Name the blood parasite species.
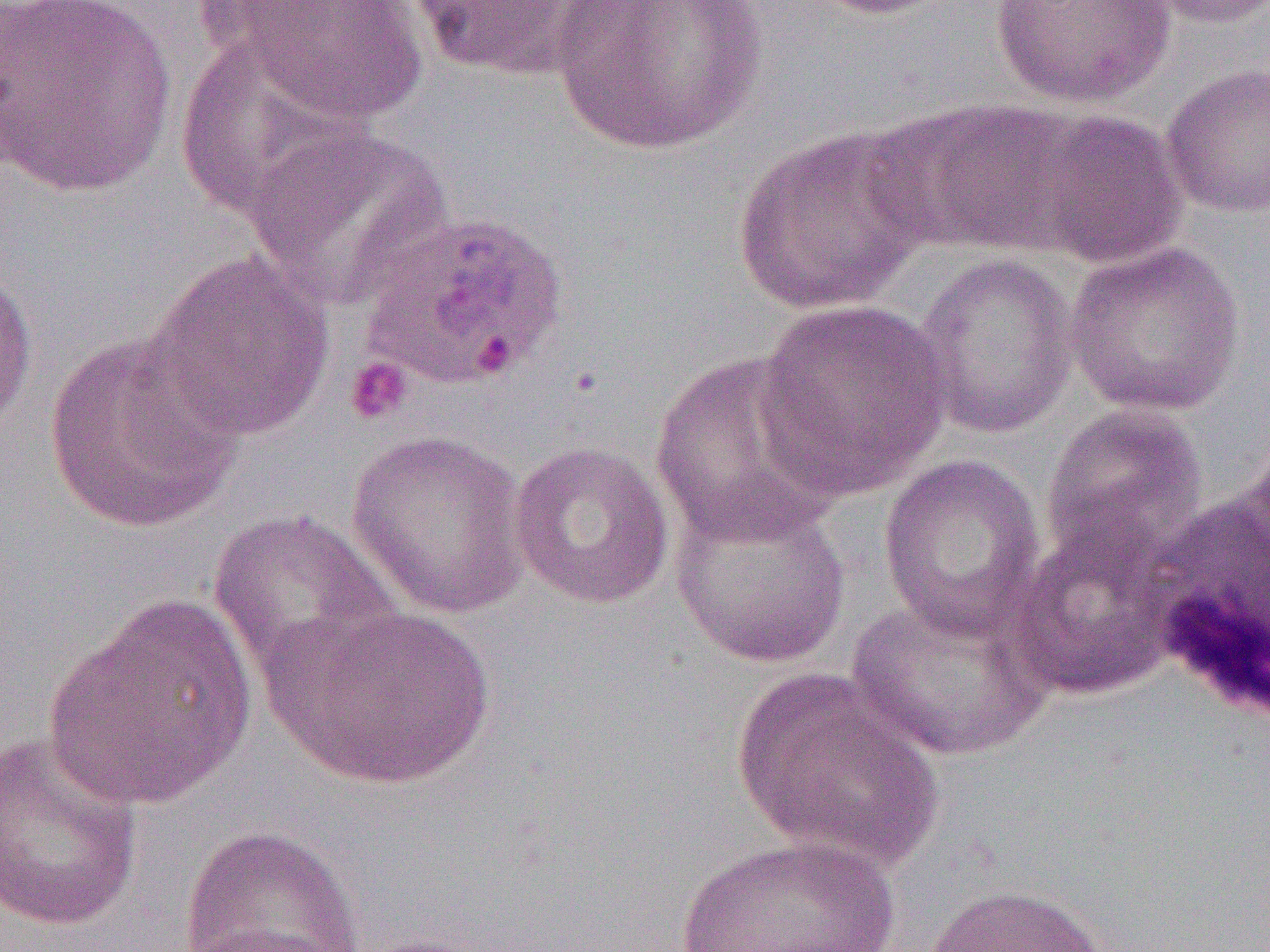

Plasmodium ovale.

magnification = 1000x
white blood cell locations = approximate bounding boxes as named x1/y1/x2/y2 corners in pixels: (x1=1135, y1=479, x2=1270, y2=723)
platelet locations = approximate bounding boxes as named x1/y1/x2/y2 corners in pixels: (x1=344, y1=356, x2=413, y2=425)
uninfected red blood cell locations = approximate bounding boxes as named x1/y1/x2/y2 corners in pixels: (x1=0, y1=0, x2=178, y2=197), (x1=221, y1=0, x2=432, y2=127), (x1=409, y1=0, x2=606, y2=79), (x1=548, y1=0, x2=769, y2=157), (x1=806, y1=0, x2=958, y2=20), (x1=988, y1=0, x2=1178, y2=109), (x1=1138, y1=0, x2=1270, y2=30), (x1=174, y1=33, x2=365, y2=222), (x1=1160, y1=61, x2=1270, y2=219), (x1=865, y1=99, x2=1077, y2=255), (x1=1020, y1=108, x2=1189, y2=269), (x1=245, y1=124, x2=454, y2=310), (x1=732, y1=124, x2=933, y2=317), (x1=1062, y1=240, x2=1245, y2=417), (x1=146, y1=248, x2=336, y2=442), (x1=911, y1=252, x2=1081, y2=440), (x1=0, y1=263, x2=38, y2=435), (x1=752, y1=299, x2=953, y2=499), (x1=43, y1=331, x2=246, y2=535), (x1=649, y1=350, x2=846, y2=547), (x1=1039, y1=404, x2=1209, y2=573), (x1=347, y1=429, x2=532, y2=619), (x1=508, y1=440, x2=676, y2=610), (x1=877, y1=453, x2=1046, y2=640), (x1=668, y1=487, x2=853, y2=670), (x1=208, y1=508, x2=401, y2=682), (x1=1009, y1=522, x2=1180, y2=702), (x1=845, y1=591, x2=1056, y2=763), (x1=43, y1=593, x2=259, y2=814), (x1=265, y1=601, x2=497, y2=791), (x1=730, y1=668, x2=945, y2=872), (x1=0, y1=731, x2=145, y2=933), (x1=175, y1=823, x2=368, y2=951), (x1=673, y1=833, x2=904, y2=952), (x1=920, y1=882, x2=1114, y2=952), (x1=346, y1=933, x2=502, y2=952)
Plasmodium ovale-infected red blood cell locations = approximate bounding boxes as named x1/y1/x2/y2 corners in pixels: (x1=360, y1=209, x2=571, y2=391)
preparation = thin blood film
image size = 1270×952 pixels
modality = light microscopy
field of view = single